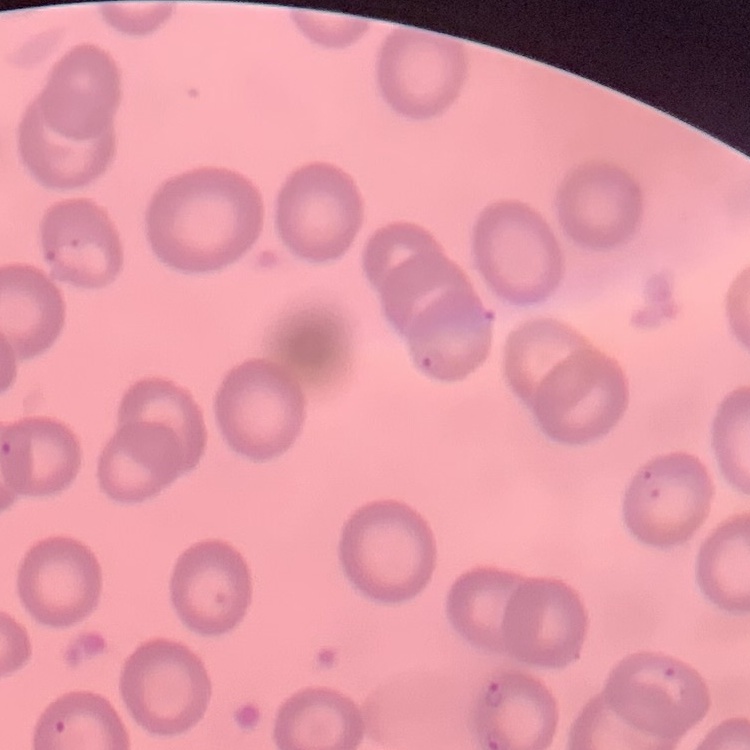

The erythrocytes show no rouleaux formation. Field's or Giemsa stain. Thin blood smear. One tile cut from a larger photomicrograph.